Outline each blood parasite and name the species.
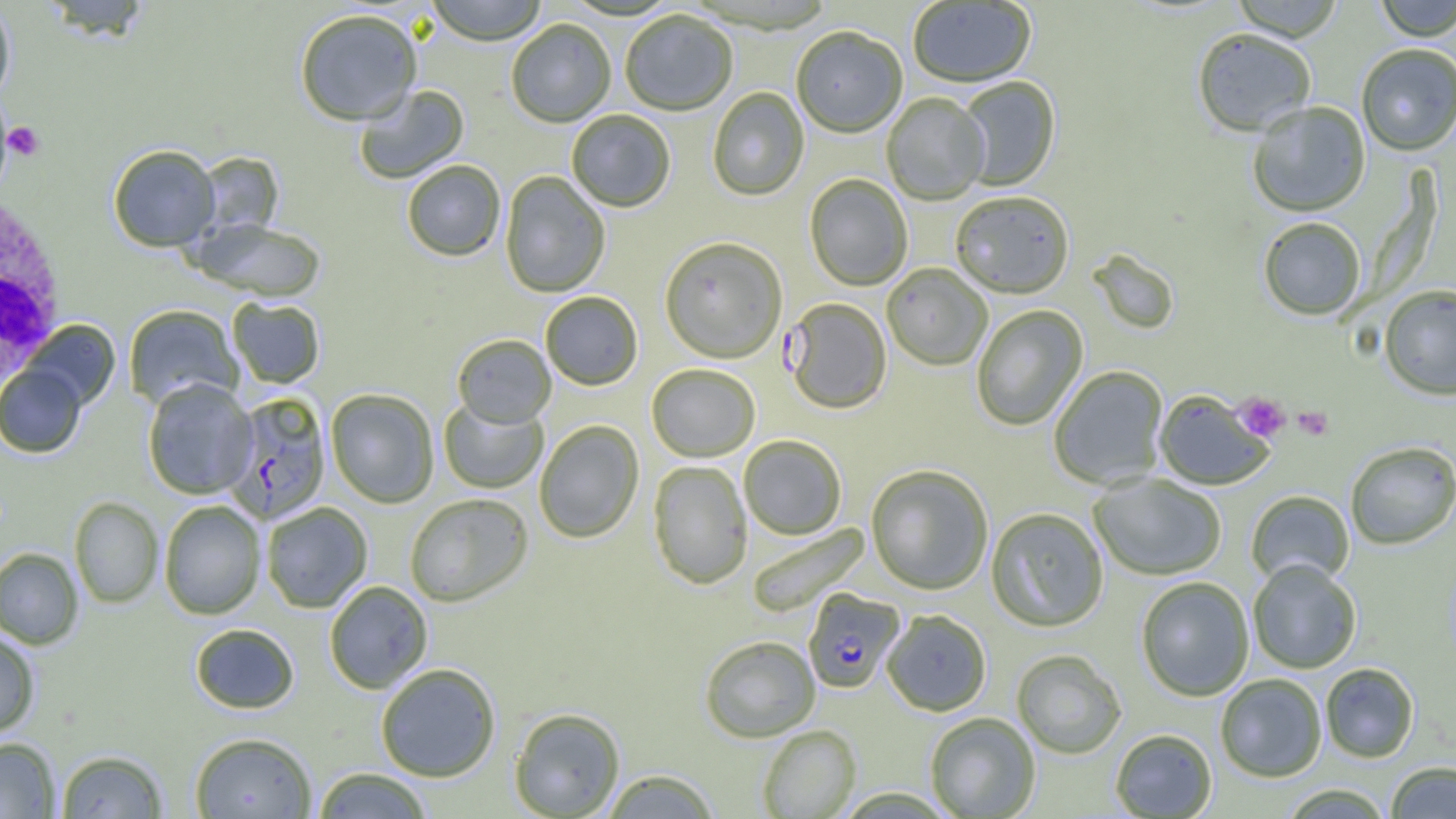

Approximate bounding boxes as named x1/y1/x2/y2 corners in pixels.
Plasmodium falciparum-infected red blood cells: (x1=783, y1=299, x2=891, y2=415), (x1=224, y1=394, x2=331, y2=524), (x1=802, y1=588, x2=905, y2=693).
No Plasmodium ovale, Plasmodium malariae, Plasmodium vivax, Babesia divergens, or Trypanosoma brucei observed.

White blood cell locations: (x1=0, y1=191, x2=68, y2=389). Platelet locations: (x1=5, y1=122, x2=45, y2=162), (x1=1233, y1=392, x2=1291, y2=442), (x1=1293, y1=406, x2=1333, y2=440). Uninfected red blood cell locations: (x1=40, y1=0, x2=151, y2=42), (x1=425, y1=0, x2=547, y2=47), (x1=1374, y1=0, x2=1456, y2=42), (x1=908, y1=1, x2=1036, y2=89), (x1=1231, y1=1, x2=1345, y2=43), (x1=0, y1=2, x2=16, y2=106), (x1=295, y1=12, x2=422, y2=128), (x1=620, y1=12, x2=737, y2=117), (x1=506, y1=21, x2=616, y2=128), (x1=791, y1=28, x2=907, y2=140), (x1=1192, y1=29, x2=1316, y2=138), (x1=1356, y1=45, x2=1456, y2=156), (x1=957, y1=77, x2=1061, y2=192), (x1=355, y1=85, x2=470, y2=185), (x1=707, y1=88, x2=809, y2=202), (x1=882, y1=94, x2=989, y2=206), (x1=1248, y1=102, x2=1370, y2=218), (x1=567, y1=110, x2=676, y2=213), (x1=108, y1=145, x2=220, y2=252), (x1=197, y1=152, x2=283, y2=238), (x1=402, y1=161, x2=506, y2=262), (x1=500, y1=172, x2=610, y2=298), (x1=804, y1=175, x2=913, y2=291), (x1=950, y1=193, x2=1074, y2=300), (x1=1258, y1=218, x2=1367, y2=321), (x1=194, y1=219, x2=326, y2=303), (x1=659, y1=239, x2=787, y2=365), (x1=1087, y1=250, x2=1180, y2=336), (x1=882, y1=264, x2=992, y2=371), (x1=1379, y1=286, x2=1456, y2=400), (x1=541, y1=292, x2=643, y2=391), (x1=227, y1=298, x2=325, y2=389), (x1=123, y1=305, x2=243, y2=411), (x1=971, y1=305, x2=1087, y2=431), (x1=23, y1=320, x2=120, y2=410), (x1=452, y1=335, x2=556, y2=428), (x1=0, y1=365, x2=86, y2=458), (x1=647, y1=365, x2=760, y2=462), (x1=1049, y1=366, x2=1168, y2=490), (x1=142, y1=379, x2=257, y2=499), (x1=325, y1=390, x2=439, y2=508), (x1=1154, y1=390, x2=1275, y2=491), (x1=439, y1=399, x2=548, y2=494), (x1=534, y1=420, x2=644, y2=544), (x1=739, y1=436, x2=847, y2=540), (x1=1345, y1=441, x2=1456, y2=550), (x1=648, y1=461, x2=752, y2=589), (x1=866, y1=465, x2=993, y2=595), (x1=1089, y1=474, x2=1227, y2=581), (x1=1246, y1=490, x2=1354, y2=588), (x1=404, y1=495, x2=533, y2=607), (x1=69, y1=497, x2=163, y2=608), (x1=159, y1=500, x2=265, y2=620), (x1=261, y1=503, x2=372, y2=613), (x1=986, y1=508, x2=1108, y2=633), (x1=747, y1=523, x2=871, y2=617), (x1=0, y1=547, x2=83, y2=650), (x1=1248, y1=559, x2=1362, y2=674), (x1=1137, y1=577, x2=1254, y2=701), (x1=324, y1=581, x2=433, y2=694), (x1=882, y1=610, x2=991, y2=717), (x1=190, y1=623, x2=299, y2=714), (x1=0, y1=629, x2=40, y2=738), (x1=699, y1=636, x2=821, y2=743), (x1=1011, y1=650, x2=1126, y2=759), (x1=375, y1=663, x2=501, y2=782), (x1=1320, y1=663, x2=1419, y2=763), (x1=1215, y1=674, x2=1327, y2=782), (x1=509, y1=707, x2=625, y2=818), (x1=924, y1=713, x2=1040, y2=818), (x1=757, y1=725, x2=860, y2=818), (x1=1110, y1=729, x2=1217, y2=818), (x1=190, y1=732, x2=317, y2=819), (x1=0, y1=737, x2=60, y2=818), (x1=56, y1=749, x2=168, y2=818), (x1=1386, y1=762, x2=1456, y2=818), (x1=311, y1=767, x2=433, y2=818), (x1=600, y1=769, x2=719, y2=818), (x1=1279, y1=784, x2=1394, y2=818), (x1=834, y1=788, x2=957, y2=818). Slide-level diagnosis: Plasmodium falciparum. Light microscopy. Image is 1456×819 pixels. Captured at 1000x magnification. One field of a larger specimen. Thin blood smear.